Identify the blood parasite species.
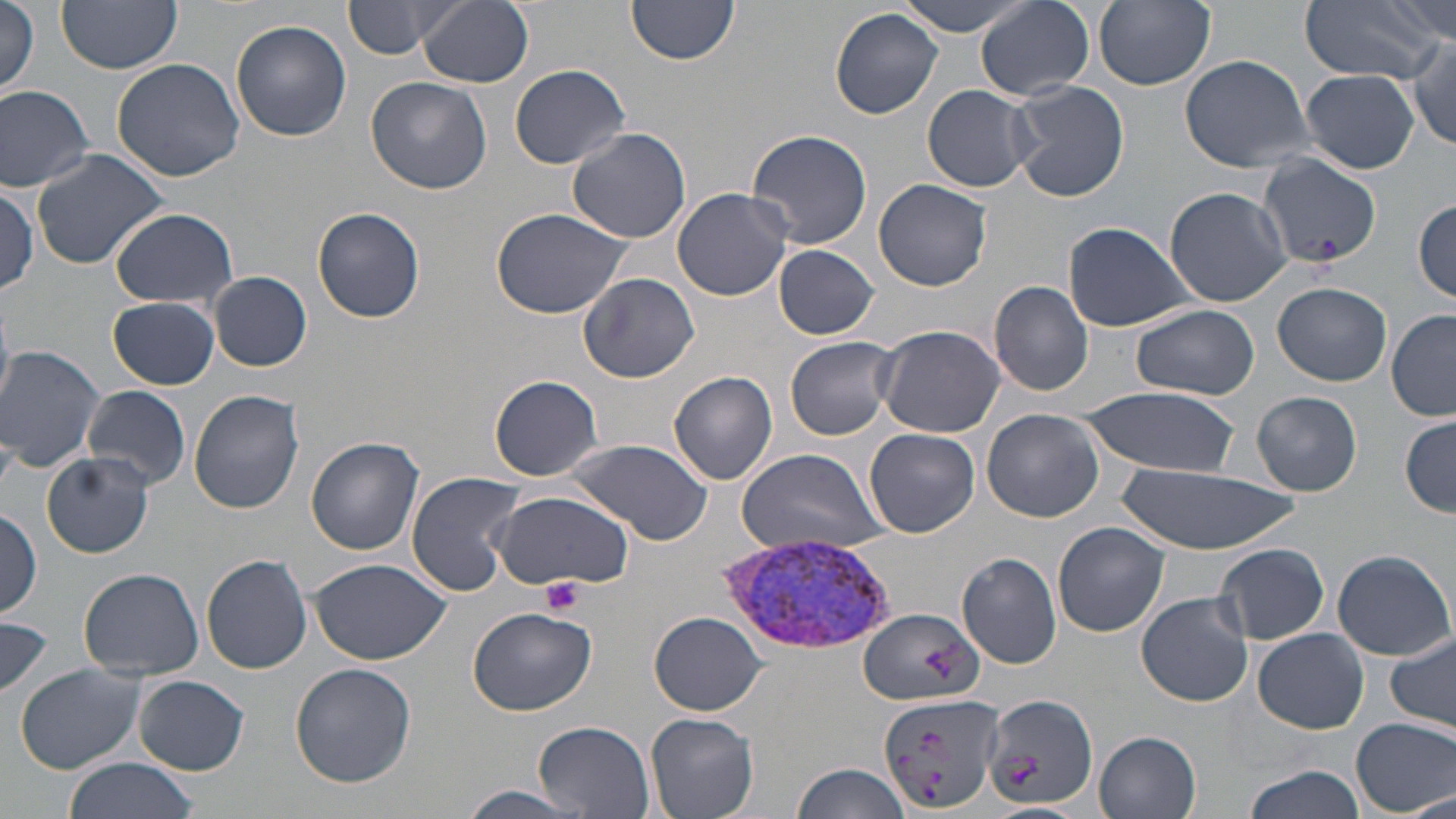
Plasmodium vivax.

Approximate bounding boxes as (x1, y1, x2, y2) in pixels. Uninfected red blood cell locations: (57, 0, 183, 73), (342, 0, 461, 59), (419, 0, 533, 88), (626, 0, 741, 65), (897, 0, 1030, 36), (976, 0, 1096, 102), (1093, 0, 1214, 90), (1297, 0, 1445, 83), (1386, 0, 1455, 44), (2, 3, 42, 96), (830, 8, 944, 119), (229, 21, 352, 141), (1407, 41, 1456, 153), (1179, 53, 1315, 173), (110, 57, 244, 182), (510, 64, 632, 170), (1300, 68, 1420, 173), (365, 74, 494, 194), (1008, 80, 1130, 203), (0, 83, 98, 192), (922, 85, 1036, 195), (566, 127, 692, 243), (745, 129, 872, 250), (30, 149, 173, 274), (1257, 156, 1380, 272), (873, 177, 995, 292), (1, 184, 41, 298), (1164, 186, 1291, 307), (672, 187, 793, 302), (1413, 198, 1455, 304), (311, 205, 426, 323), (109, 208, 238, 311), (490, 208, 635, 318), (1063, 221, 1198, 332), (772, 243, 879, 340), (209, 271, 312, 372), (578, 272, 699, 383), (989, 281, 1094, 396), (1272, 282, 1392, 386), (108, 297, 219, 389), (0, 303, 14, 411), (1128, 303, 1261, 401), (1387, 311, 1456, 421), (874, 324, 1005, 438), (785, 336, 898, 440), (1, 345, 106, 472), (669, 372, 778, 485), (490, 375, 603, 481), (80, 385, 191, 492), (1082, 387, 1242, 480), (189, 389, 305, 515), (1251, 391, 1363, 497), (981, 408, 1107, 524), (1399, 416, 1455, 518), (865, 427, 979, 538), (307, 436, 425, 554), (565, 439, 714, 547), (732, 449, 885, 558), (42, 453, 154, 558), (1122, 462, 1296, 557), (405, 471, 528, 595), (492, 490, 635, 592), (0, 508, 43, 617), (1053, 521, 1172, 638), (1214, 543, 1331, 645), (1331, 548, 1456, 659), (956, 552, 1061, 669), (202, 554, 313, 674), (311, 558, 450, 665), (78, 567, 205, 680), (1137, 592, 1254, 706), (467, 606, 598, 716), (857, 606, 984, 707), (650, 613, 767, 715), (0, 617, 52, 702), (1254, 628, 1369, 734), (1385, 632, 1456, 733), (14, 662, 146, 775), (291, 663, 417, 787), (132, 674, 249, 775), (878, 691, 1004, 814), (983, 691, 1097, 809), (643, 711, 760, 819), (1351, 716, 1455, 816), (534, 719, 655, 818), (1095, 730, 1201, 817), (63, 758, 198, 819), (789, 762, 910, 819), (1240, 764, 1367, 819), (451, 783, 592, 818), (1400, 792, 1454, 819). Plasmodium vivax-infected red blood cell locations: (720, 533, 900, 654). Platelet locations: (540, 575, 584, 615). One field of a larger specimen. Image is 1456×819 pixels. 1000x magnification. Thin blood smear. May-Grünwald-Giemsa stain. Optical microscopy.